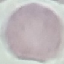

result: negative for malaria parasites
preparation: thin blood film
capture: smartphone through the microscope eyepiece
stain: Giemsa
image_type: cell patch, automatically extracted from a larger field of view and resized to 64 × 64 pixels